State the blood parasite species.
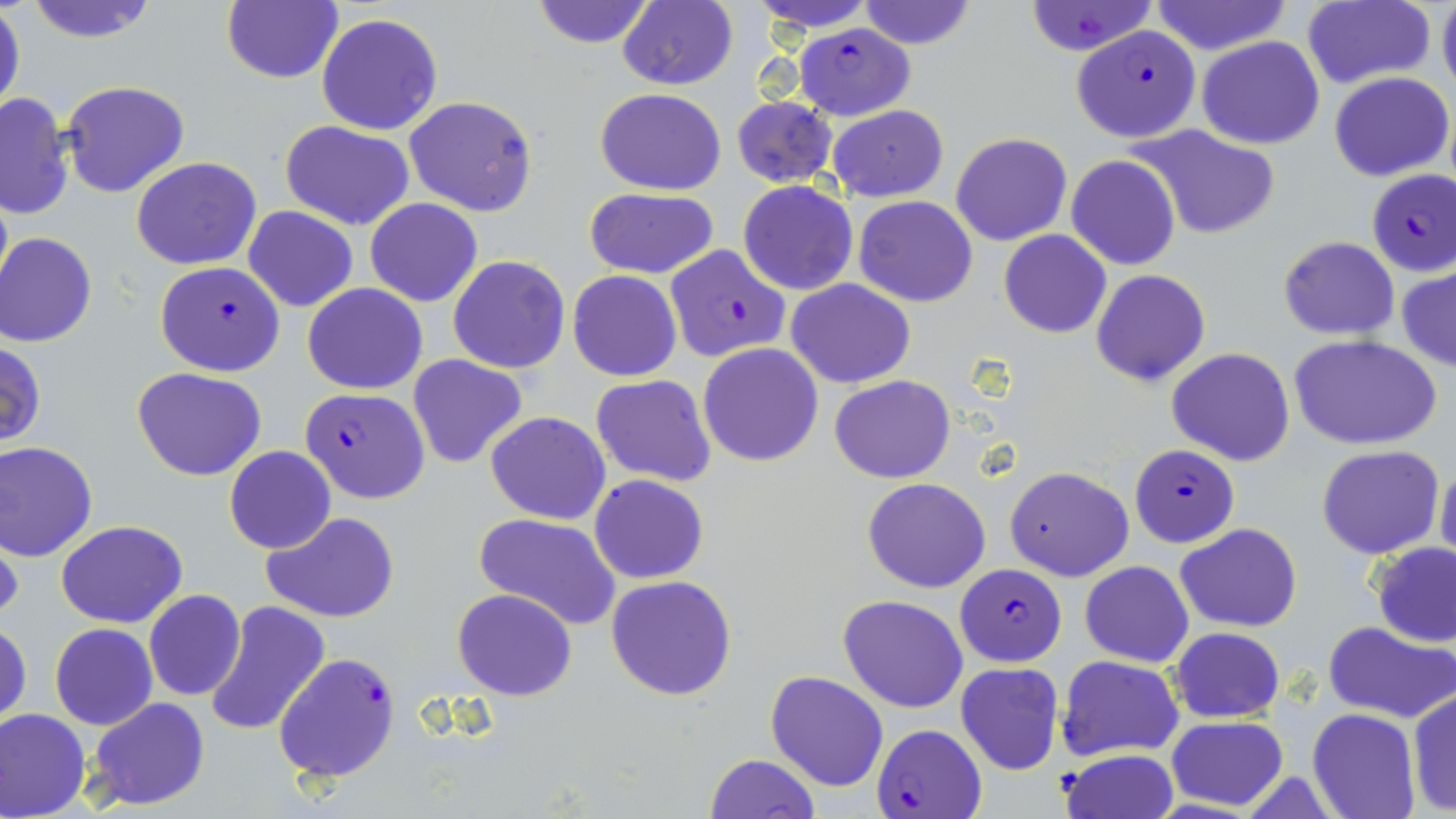

Plasmodium falciparum.

Summary:
  - Coordinate format: approximate bounding boxes as named x1/y1/x2/y2 corners in pixels
  - Uninfected red blood cell locations: (x1=22, y1=0, x2=161, y2=43), (x1=222, y1=0, x2=344, y2=84), (x1=529, y1=0, x2=656, y2=49), (x1=749, y1=0, x2=879, y2=33), (x1=856, y1=0, x2=977, y2=50), (x1=1436, y1=0, x2=1456, y2=101), (x1=617, y1=1, x2=737, y2=90), (x1=1148, y1=1, x2=1293, y2=56), (x1=1301, y1=1, x2=1435, y2=89), (x1=1023, y1=2, x2=1158, y2=56), (x1=0, y1=6, x2=24, y2=118), (x1=316, y1=13, x2=443, y2=136), (x1=1196, y1=36, x2=1325, y2=150), (x1=1328, y1=71, x2=1453, y2=182), (x1=60, y1=79, x2=190, y2=198), (x1=595, y1=89, x2=726, y2=195), (x1=1, y1=93, x2=72, y2=220), (x1=403, y1=94, x2=539, y2=216), (x1=731, y1=96, x2=837, y2=188), (x1=826, y1=106, x2=949, y2=202), (x1=281, y1=120, x2=415, y2=231), (x1=1132, y1=126, x2=1281, y2=239), (x1=952, y1=132, x2=1071, y2=245), (x1=1066, y1=155, x2=1181, y2=270), (x1=131, y1=157, x2=260, y2=270), (x1=737, y1=181, x2=859, y2=296), (x1=584, y1=188, x2=720, y2=277), (x1=854, y1=196, x2=977, y2=306), (x1=365, y1=197, x2=482, y2=307), (x1=244, y1=207, x2=358, y2=312), (x1=999, y1=230, x2=1111, y2=339), (x1=1, y1=234, x2=98, y2=348), (x1=1277, y1=235, x2=1399, y2=340), (x1=448, y1=254, x2=570, y2=374), (x1=1396, y1=264, x2=1456, y2=373), (x1=1091, y1=268, x2=1211, y2=386), (x1=569, y1=270, x2=682, y2=382), (x1=786, y1=279, x2=915, y2=387), (x1=304, y1=284, x2=426, y2=394), (x1=1289, y1=334, x2=1443, y2=451), (x1=0, y1=340, x2=47, y2=449), (x1=698, y1=342, x2=824, y2=467), (x1=1166, y1=347, x2=1295, y2=465), (x1=408, y1=355, x2=528, y2=470), (x1=133, y1=367, x2=266, y2=480), (x1=591, y1=374, x2=716, y2=488), (x1=830, y1=374, x2=955, y2=485), (x1=486, y1=411, x2=610, y2=525), (x1=0, y1=440, x2=99, y2=560), (x1=1316, y1=444, x2=1445, y2=560), (x1=224, y1=446, x2=335, y2=554), (x1=1436, y1=457, x2=1456, y2=569), (x1=1004, y1=465, x2=1133, y2=581), (x1=590, y1=474, x2=708, y2=583), (x1=862, y1=477, x2=991, y2=594), (x1=264, y1=511, x2=400, y2=623), (x1=473, y1=512, x2=621, y2=629), (x1=0, y1=518, x2=22, y2=627), (x1=55, y1=520, x2=187, y2=628), (x1=1177, y1=523, x2=1301, y2=632), (x1=1370, y1=542, x2=1455, y2=649), (x1=1080, y1=561, x2=1194, y2=666), (x1=607, y1=574, x2=736, y2=701), (x1=452, y1=588, x2=576, y2=700), (x1=143, y1=590, x2=247, y2=702), (x1=837, y1=594, x2=969, y2=713), (x1=204, y1=602, x2=331, y2=737), (x1=1, y1=620, x2=31, y2=728), (x1=1322, y1=621, x2=1456, y2=722), (x1=50, y1=623, x2=158, y2=730), (x1=1169, y1=627, x2=1285, y2=722), (x1=1056, y1=656, x2=1184, y2=760), (x1=954, y1=661, x2=1066, y2=776), (x1=766, y1=671, x2=889, y2=792), (x1=1406, y1=689, x2=1456, y2=813), (x1=87, y1=696, x2=212, y2=812), (x1=0, y1=708, x2=91, y2=818), (x1=1307, y1=709, x2=1419, y2=819), (x1=1166, y1=714, x2=1289, y2=812), (x1=1059, y1=749, x2=1178, y2=818), (x1=702, y1=753, x2=820, y2=819)
  - Plasmodium falciparum-infected red blood cell locations: (x1=792, y1=25, x2=916, y2=119), (x1=1073, y1=25, x2=1200, y2=143), (x1=1366, y1=168, x2=1456, y2=275), (x1=664, y1=244, x2=790, y2=362), (x1=155, y1=261, x2=285, y2=377), (x1=299, y1=388, x2=428, y2=504), (x1=1129, y1=444, x2=1239, y2=547), (x1=955, y1=564, x2=1067, y2=667), (x1=271, y1=652, x2=400, y2=782), (x1=872, y1=723, x2=987, y2=818)
  - Preparation: thin blood smear
  - Stain: May-Grünwald-Giemsa
  - Magnification: 1000x
  - Field of view: one of a larger specimen
  - Image size: 1456×819 pixels
  - Modality: light microscopy